Identify the cell.
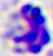

A leukocyte.

Captured at 400x magnification. Micrograph.